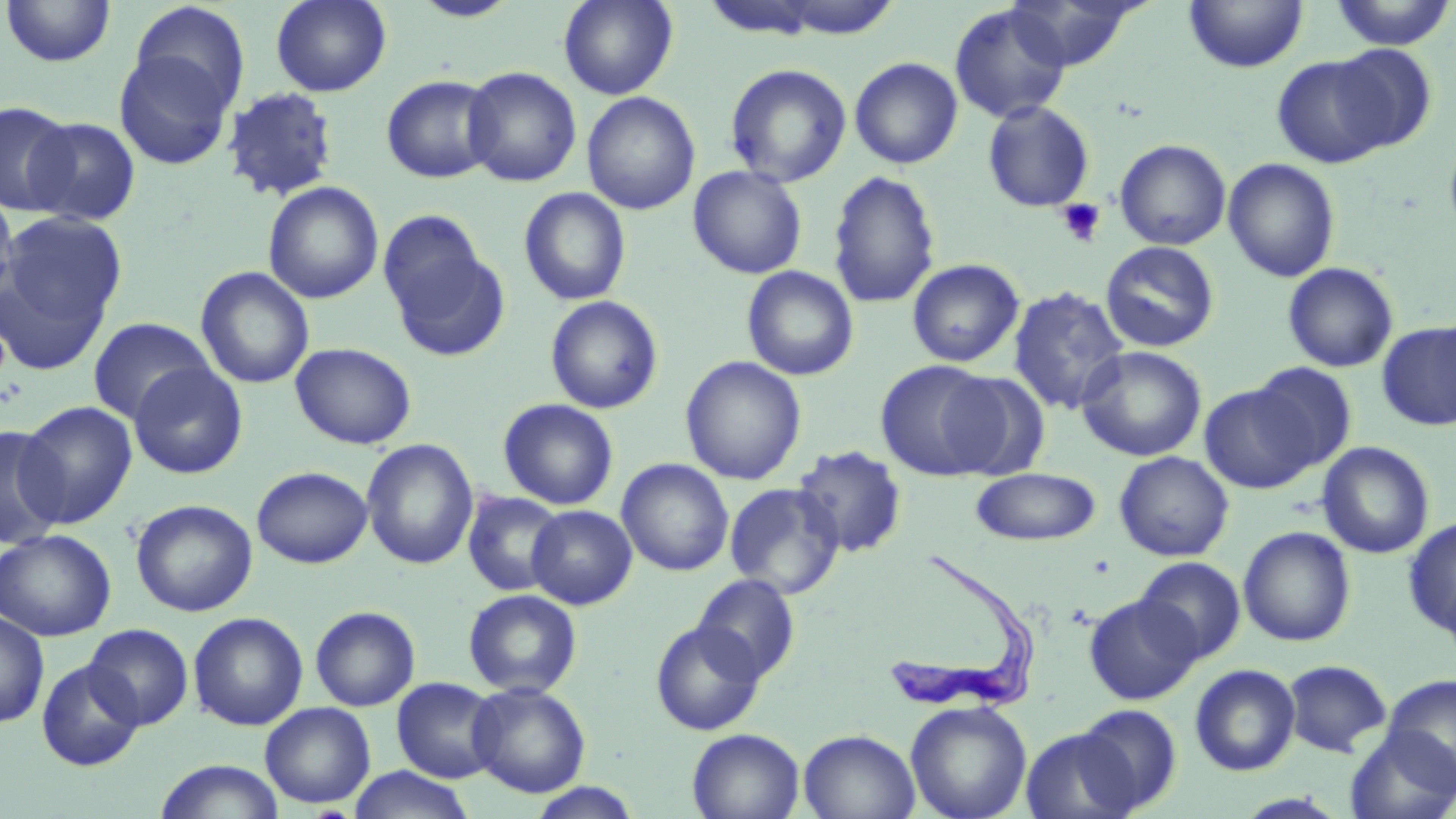
{
  "slide_level_diagnosis": "Trypanosoma brucei",
  "field_of_view": "single",
  "preparation": "thin blood film",
  "image_size": "1456×819 pixels",
  "uninfected_red_blood_cell_locations": "approximate bounding boxes as (x1, y1, x2, y2) in pixels: (270, 0, 392, 97), (408, 0, 522, 23), (559, 0, 678, 99), (1004, 0, 1145, 71), (1184, 0, 1309, 74), (1329, 0, 1455, 50), (1, 1, 116, 68), (129, 1, 250, 115), (949, 3, 1071, 124), (1330, 44, 1437, 152), (113, 48, 237, 171), (1272, 55, 1394, 168), (849, 57, 963, 169), (724, 63, 852, 187), (462, 66, 582, 187), (381, 74, 499, 183), (222, 88, 339, 202), (582, 91, 701, 215), (1, 100, 76, 216), (982, 101, 1095, 213), (25, 116, 141, 226), (1444, 136, 1456, 242), (1115, 139, 1231, 250), (1223, 158, 1340, 282), (688, 164, 808, 279), (827, 170, 941, 309), (263, 181, 384, 304), (0, 185, 20, 310), (518, 187, 632, 306), (2, 210, 127, 336), (378, 215, 507, 362), (1100, 241, 1219, 352), (0, 257, 114, 378), (907, 258, 1024, 367), (1282, 262, 1399, 372), (195, 266, 315, 389), (741, 266, 858, 380), (1007, 286, 1130, 415), (545, 295, 663, 414), (87, 317, 216, 424), (1376, 322, 1456, 431), (290, 342, 417, 449), (1076, 346, 1207, 461), (680, 356, 806, 485), (875, 360, 1001, 481), (128, 362, 248, 479), (1248, 362, 1358, 472), (940, 371, 1050, 478), (1200, 382, 1320, 494), (498, 398, 619, 510), (17, 400, 138, 528), (0, 425, 66, 550), (361, 439, 479, 570), (1317, 442, 1435, 558), (791, 445, 908, 559), (1114, 451, 1234, 561), (616, 458, 734, 576), (251, 466, 373, 568), (970, 467, 1101, 546), (724, 482, 845, 599), (462, 490, 567, 597), (131, 499, 258, 616), (526, 505, 637, 610), (1403, 516, 1456, 637), (1238, 526, 1356, 647), (0, 529, 117, 641), (1135, 556, 1246, 663), (691, 574, 801, 684), (463, 589, 582, 698), (1083, 593, 1202, 705), (309, 605, 421, 711), (0, 610, 50, 728), (188, 611, 308, 731), (649, 619, 767, 737), (84, 623, 194, 730), (36, 658, 144, 772), (1282, 659, 1392, 757), (1189, 664, 1301, 776), (1382, 673, 1456, 789), (391, 677, 504, 783), (467, 682, 591, 798), (905, 700, 1033, 819), (260, 702, 376, 808), (1075, 703, 1183, 814), (1020, 727, 1141, 819), (1344, 727, 1456, 819), (687, 728, 806, 819), (799, 729, 921, 819), (152, 758, 286, 818), (346, 766, 476, 819), (526, 782, 643, 819), (1229, 792, 1352, 818)",
  "platelet_locations": "approximate bounding boxes as (x1, y1, x2, y2) in pixels: (1056, 198, 1106, 246)",
  "modality": "light microscopy",
  "magnification": "1000x",
  "stain": "May-Grünwald-Giemsa",
  "trypanosoma_brucei_locations": "approximate bounding boxes as (x1, y1, x2, y2) in pixels: (886, 555, 1036, 717)"
}